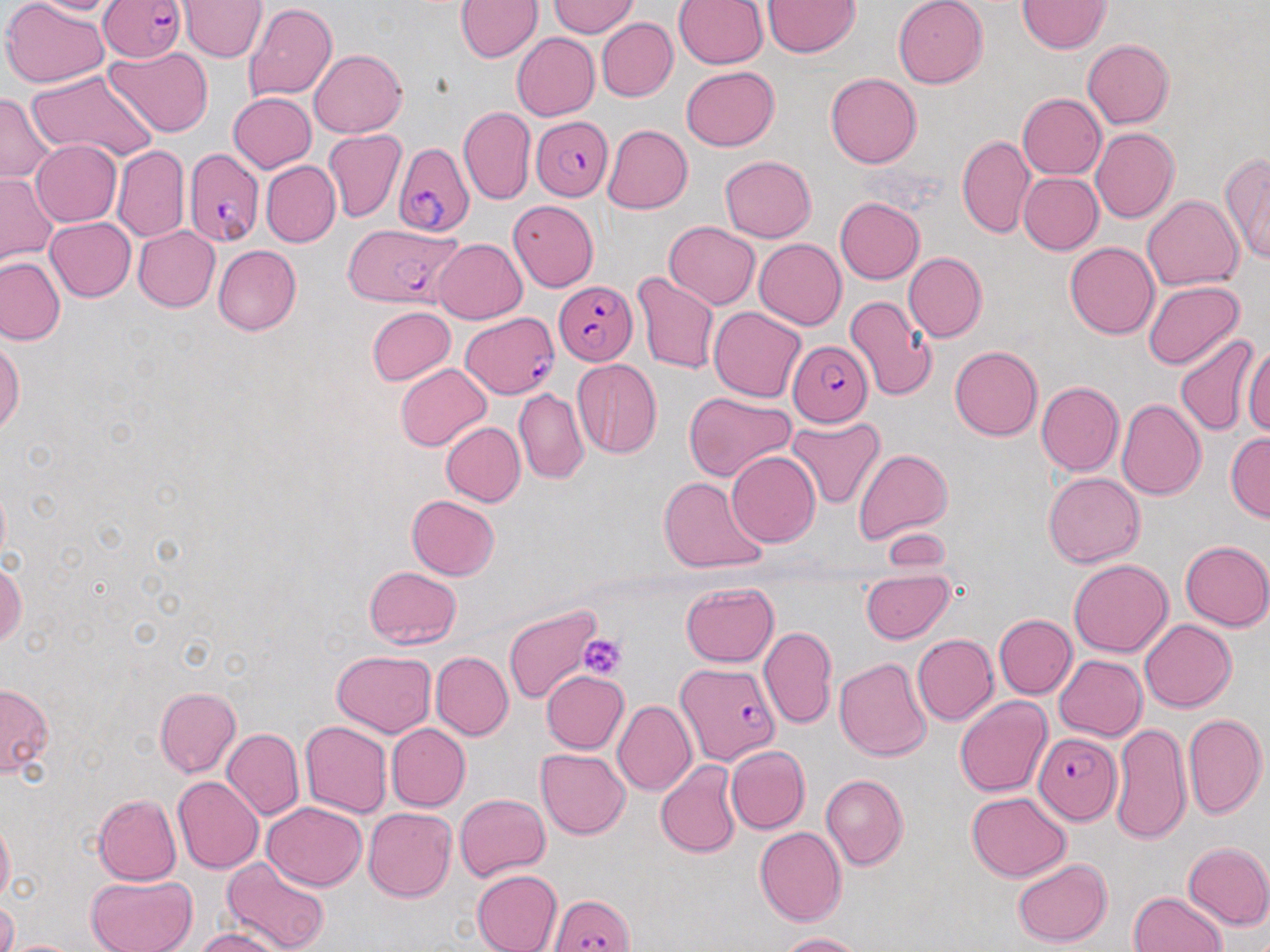
slide-level diagnosis = Plasmodium falciparum
magnification = 1000x
field of view = single
preparation = thin blood smear
platelet locations = approximate bounding boxes as named x1/y1/x2/y2 corners in pixels: (x1=580, y1=633, x2=627, y2=682)
image size = 1270×952 pixels
stain = May-Grünwald-Giemsa
modality = light microscopy
uninfected red blood cell locations = approximate bounding boxes as named x1/y1/x2/y2 corners in pixels: (x1=1, y1=0, x2=110, y2=87), (x1=17, y1=0, x2=126, y2=16), (x1=178, y1=0, x2=268, y2=63), (x1=673, y1=0, x2=769, y2=69), (x1=763, y1=0, x2=861, y2=58), (x1=893, y1=0, x2=987, y2=88), (x1=1017, y1=0, x2=1111, y2=53), (x1=454, y1=1, x2=542, y2=62), (x1=547, y1=2, x2=639, y2=36), (x1=244, y1=3, x2=337, y2=100), (x1=596, y1=18, x2=678, y2=102), (x1=512, y1=32, x2=600, y2=121), (x1=1082, y1=39, x2=1173, y2=128), (x1=105, y1=46, x2=212, y2=137), (x1=308, y1=49, x2=407, y2=137), (x1=682, y1=66, x2=779, y2=150), (x1=26, y1=68, x2=156, y2=164), (x1=825, y1=73, x2=922, y2=169), (x1=0, y1=90, x2=55, y2=183), (x1=228, y1=92, x2=317, y2=173), (x1=1017, y1=94, x2=1106, y2=179), (x1=458, y1=106, x2=535, y2=205), (x1=603, y1=125, x2=692, y2=214), (x1=1090, y1=128, x2=1179, y2=224), (x1=324, y1=129, x2=407, y2=223), (x1=957, y1=133, x2=1033, y2=238), (x1=31, y1=140, x2=121, y2=227), (x1=113, y1=145, x2=190, y2=243), (x1=720, y1=155, x2=816, y2=242), (x1=1221, y1=155, x2=1270, y2=263), (x1=261, y1=161, x2=341, y2=247), (x1=0, y1=173, x2=58, y2=266), (x1=1018, y1=173, x2=1103, y2=255), (x1=1141, y1=195, x2=1244, y2=291), (x1=835, y1=196, x2=924, y2=284), (x1=508, y1=200, x2=599, y2=292), (x1=45, y1=216, x2=137, y2=302), (x1=664, y1=221, x2=760, y2=309), (x1=133, y1=226, x2=220, y2=312), (x1=433, y1=238, x2=527, y2=324), (x1=754, y1=238, x2=846, y2=329), (x1=1066, y1=242, x2=1160, y2=339), (x1=213, y1=244, x2=301, y2=336), (x1=903, y1=252, x2=987, y2=342), (x1=0, y1=256, x2=65, y2=345), (x1=631, y1=271, x2=720, y2=375), (x1=1143, y1=281, x2=1246, y2=370), (x1=845, y1=294, x2=938, y2=403), (x1=708, y1=305, x2=806, y2=402), (x1=366, y1=306, x2=456, y2=386), (x1=1175, y1=333, x2=1261, y2=436), (x1=1241, y1=338, x2=1270, y2=438), (x1=0, y1=339, x2=23, y2=436), (x1=949, y1=346, x2=1043, y2=441), (x1=572, y1=358, x2=662, y2=458), (x1=395, y1=363, x2=492, y2=452), (x1=1036, y1=381, x2=1124, y2=475), (x1=513, y1=388, x2=589, y2=484), (x1=683, y1=392, x2=795, y2=482), (x1=1117, y1=397, x2=1206, y2=499), (x1=785, y1=418, x2=885, y2=511), (x1=440, y1=422, x2=525, y2=507), (x1=1225, y1=432, x2=1270, y2=522), (x1=852, y1=447, x2=953, y2=545), (x1=726, y1=451, x2=820, y2=548), (x1=1044, y1=472, x2=1145, y2=567), (x1=659, y1=476, x2=769, y2=575), (x1=406, y1=494, x2=499, y2=579), (x1=882, y1=527, x2=952, y2=573), (x1=1180, y1=540, x2=1270, y2=631), (x1=1069, y1=559, x2=1173, y2=657), (x1=0, y1=562, x2=27, y2=646), (x1=363, y1=566, x2=461, y2=649), (x1=861, y1=570, x2=954, y2=643), (x1=680, y1=581, x2=778, y2=667), (x1=504, y1=605, x2=602, y2=704), (x1=994, y1=615, x2=1076, y2=698), (x1=1139, y1=619, x2=1237, y2=712), (x1=760, y1=626, x2=837, y2=730), (x1=912, y1=634, x2=998, y2=724), (x1=775, y1=637, x2=892, y2=746), (x1=331, y1=650, x2=438, y2=736), (x1=431, y1=651, x2=513, y2=740), (x1=1053, y1=655, x2=1146, y2=741), (x1=834, y1=656, x2=932, y2=761), (x1=540, y1=670, x2=629, y2=753), (x1=0, y1=683, x2=53, y2=778), (x1=154, y1=686, x2=241, y2=778), (x1=954, y1=696, x2=1052, y2=797), (x1=613, y1=700, x2=696, y2=797), (x1=1183, y1=713, x2=1267, y2=819), (x1=300, y1=720, x2=393, y2=818), (x1=386, y1=723, x2=471, y2=811), (x1=1112, y1=723, x2=1192, y2=845), (x1=222, y1=728, x2=304, y2=820), (x1=725, y1=745, x2=809, y2=834), (x1=535, y1=748, x2=630, y2=838), (x1=656, y1=760, x2=741, y2=858), (x1=821, y1=773, x2=909, y2=871), (x1=172, y1=776, x2=264, y2=875), (x1=965, y1=792, x2=1072, y2=881), (x1=456, y1=793, x2=550, y2=879), (x1=94, y1=794, x2=182, y2=885), (x1=261, y1=802, x2=367, y2=890), (x1=363, y1=807, x2=456, y2=902), (x1=0, y1=818, x2=14, y2=902), (x1=754, y1=827, x2=846, y2=927), (x1=1183, y1=842, x2=1270, y2=930), (x1=222, y1=858, x2=332, y2=952), (x1=1013, y1=858, x2=1113, y2=948), (x1=471, y1=869, x2=562, y2=952), (x1=86, y1=875, x2=196, y2=952), (x1=1128, y1=890, x2=1229, y2=952), (x1=1, y1=898, x2=18, y2=952), (x1=195, y1=929, x2=285, y2=952), (x1=775, y1=932, x2=865, y2=951), (x1=3, y1=938, x2=87, y2=951)
Plasmodium falciparum-infected red blood cell locations = approximate bounding boxes as named x1/y1/x2/y2 corners in pixels: (x1=99, y1=0, x2=186, y2=63), (x1=531, y1=117, x2=615, y2=202), (x1=394, y1=142, x2=475, y2=237), (x1=184, y1=148, x2=265, y2=247), (x1=344, y1=223, x2=464, y2=308), (x1=554, y1=281, x2=639, y2=364), (x1=461, y1=312, x2=558, y2=399), (x1=787, y1=340, x2=874, y2=428), (x1=677, y1=662, x2=780, y2=766), (x1=1033, y1=733, x2=1121, y2=825), (x1=549, y1=894, x2=634, y2=952)